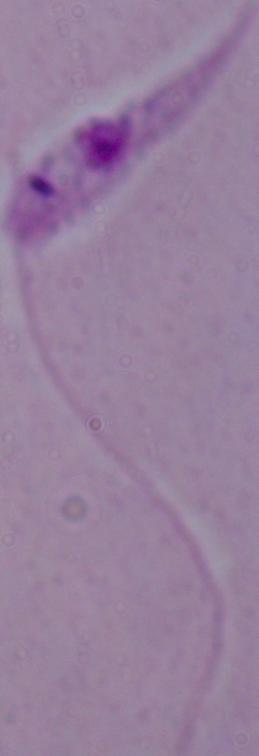

modality = micrograph
magnification = 1000x
identification = Leishmania